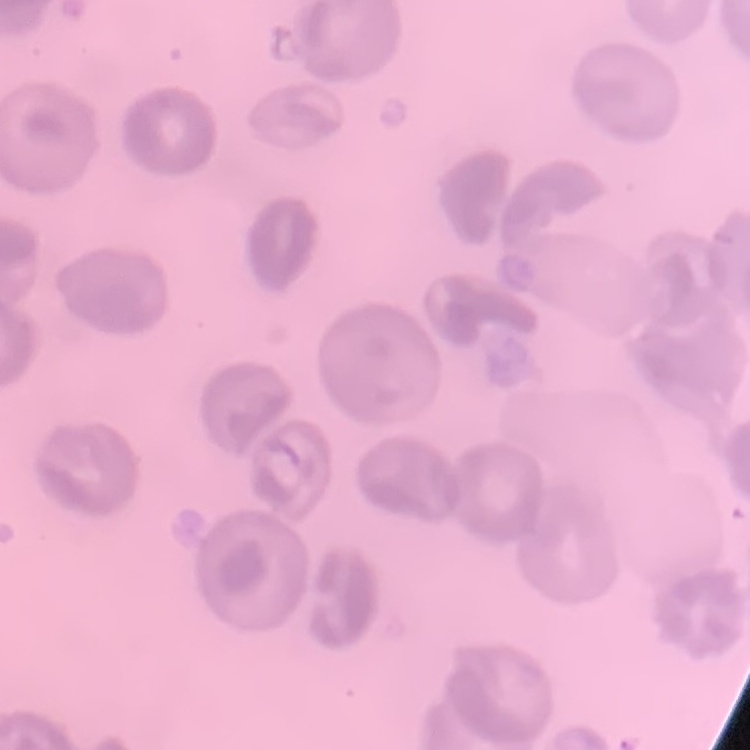
Summary:
  - Red blood cell morphology: no rouleaux formation
  - Image type: one tile cut from a larger photomicrograph
  - Preparation: thin peripheral smear
  - Stain: Field's or Giemsa